Name the parasite shown.
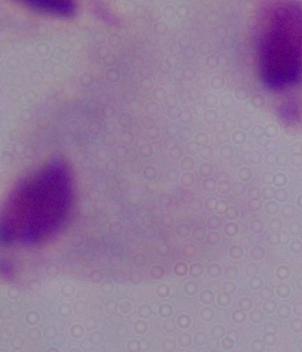

This is a trichomonad.

Summary:
  - Magnification: 1000x
  - Modality: micrograph